Report the malaria status of this cell.
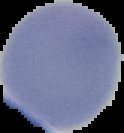
It is uninfected.

{
  "image_size": "124×133 pixels",
  "preparation": "thin blood film",
  "image_type": "segmented cell region on a black background"
}